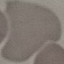

malaria status = uninfected
image type = cell patch, automatically extracted from a larger field of view and resized to 64 × 64 pixels
stain = Giemsa
capture = smartphone camera at the microscope eyepiece
preparation = thin blood film